Comment on the morphology of the red blood cells.
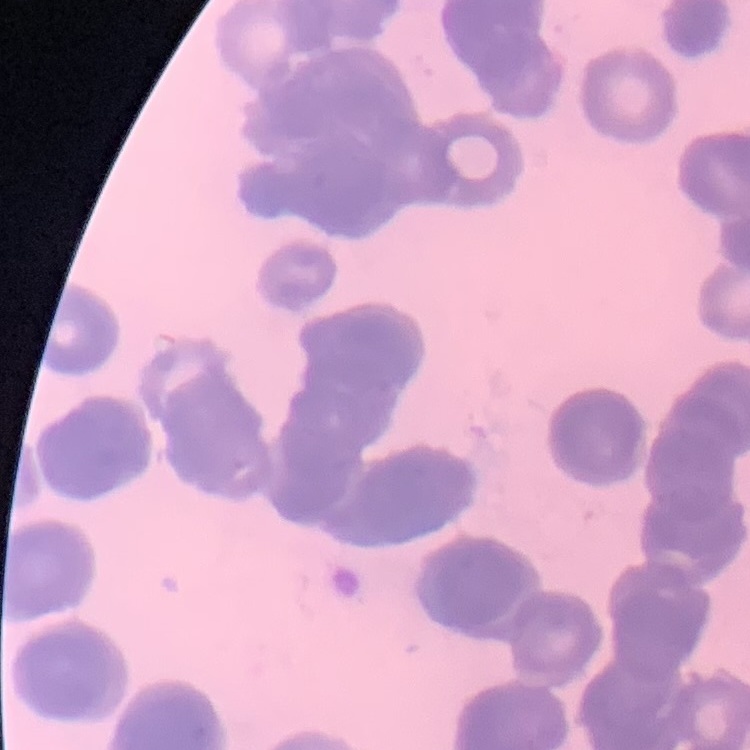

They show rouleaux formation.

preparation = thin peripheral smear
image type = square crop of a larger photomicrograph
stain = Field's or Giemsa